Point out each Plasmodium parasite.
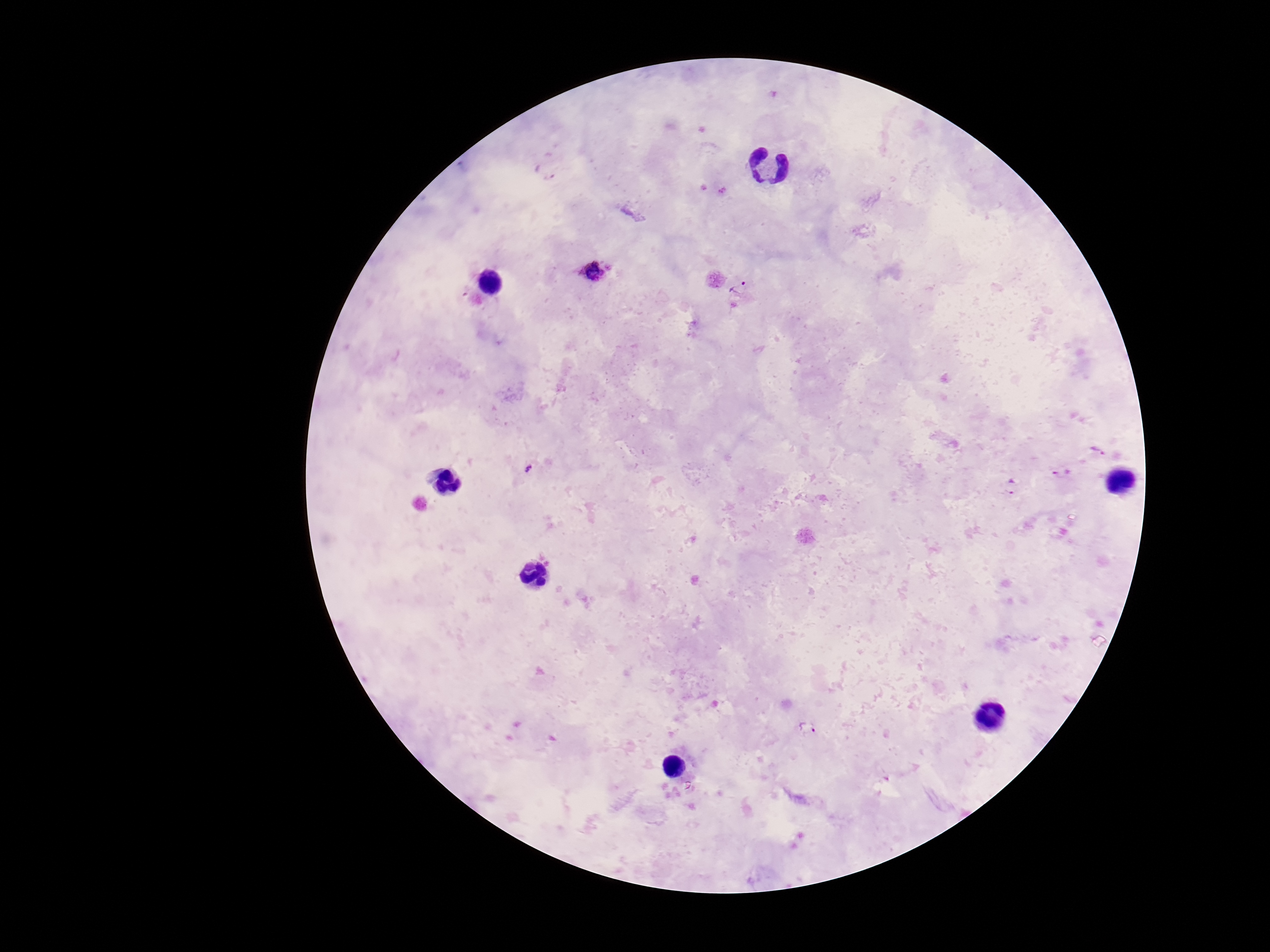
Approximate centers as [x, y] in pixels.
Plasmodium parasites: [546, 171], [594, 270], [741, 288], [1099, 452], [529, 469], [1062, 473], [1011, 487], [807, 726].

Thick blood smear. 100x magnification. Smartphone photograph taken through the microscope eyepiece. One field from this slide. Giemsa-stained preparation. Patient malaria status: infected. Image is 1270×952 pixels.